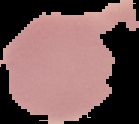

Result: no Plasmodium parasites seen. Segmented cell region on a black background. Image is 139×124 pixels. From a thin blood smear.